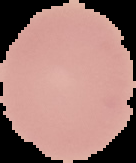
image size = 136×163 pixels
preparation = thin blood film
image type = segmented cell region with the area outside set to black
malaria status = uninfected